Report the malaria status of this cell.
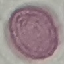
It is uninfected.

Summary:
  - Stain: Giemsa
  - Image type: cell patch, automatically extracted from a larger field of view and resized to 64 × 64 pixels
  - Preparation: thin blood smear
  - Capture: smartphone camera at the microscope eyepiece